State which parasite is depicted.
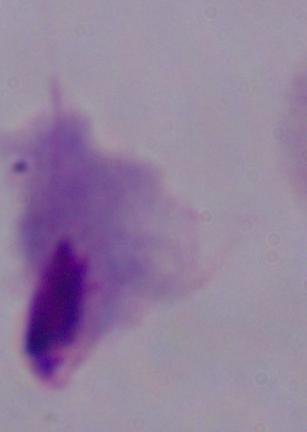
This is a trichomonad.

magnification = 1000x
modality = photomicrograph